Locate every uninfected red blood cell.
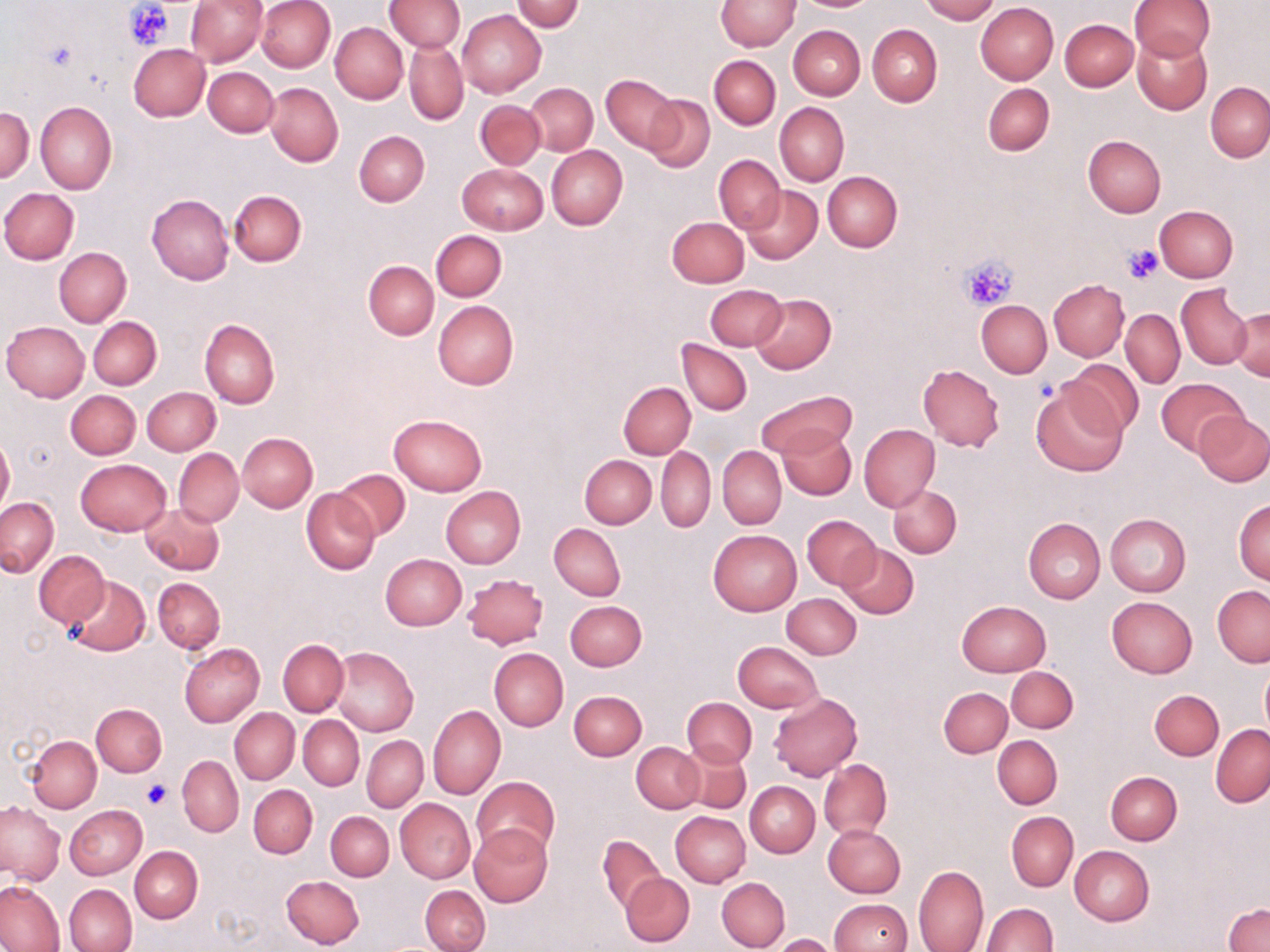
Approximate bounding boxes as (x1,y1)-(x2,y2) corner pairs in pixels.
Uninfected red blood cells: (185,0)-(266,66), (256,0)-(335,72), (920,0)-(998,23), (1130,0)-(1215,62), (384,1)-(464,53), (512,1)-(584,32), (715,1)-(799,50), (976,3)-(1059,84), (458,9)-(546,97), (1060,18)-(1138,91), (330,22)-(408,103), (789,25)-(865,99), (867,25)-(942,106), (1133,35)-(1213,115), (405,39)-(468,126), (128,44)-(210,121), (709,55)-(779,129), (204,67)-(278,137), (601,75)-(680,153), (982,82)-(1055,156), (1205,82)-(1270,162), (265,83)-(343,167), (526,83)-(597,155), (643,94)-(714,172), (475,100)-(545,169), (35,101)-(115,194), (775,102)-(849,186), (0,106)-(32,184), (354,130)-(430,206), (1083,135)-(1166,216), (546,145)-(627,229), (714,155)-(785,233), (457,164)-(548,235), (822,171)-(902,252), (742,185)-(822,263), (0,188)-(78,264), (227,190)-(306,267), (146,194)-(234,284), (1154,205)-(1238,282), (666,216)-(749,286), (431,230)-(507,301), (53,247)-(131,328), (364,260)-(439,339), (1049,280)-(1128,360), (705,283)-(787,350), (1176,284)-(1252,369), (750,293)-(836,374), (976,299)-(1052,378), (433,301)-(519,390), (1230,306)-(1269,381), (1121,308)-(1185,388), (88,317)-(162,389), (199,319)-(279,408), (1,321)-(90,402), (677,339)-(752,416), (1063,359)-(1142,438), (916,365)-(1004,451), (1156,377)-(1247,456), (617,381)-(696,459), (1031,385)-(1125,476), (142,386)-(220,455), (756,389)-(855,460), (65,390)-(140,459), (68,391)-(147,529), (1195,410)-(1270,486), (389,413)-(488,496), (859,424)-(940,511), (779,427)-(855,500), (237,432)-(317,512), (0,435)-(14,516), (718,446)-(786,529), (656,447)-(715,533), (174,449)-(243,526), (580,454)-(656,529), (75,459)-(171,536), (333,468)-(410,540), (889,485)-(961,558), (440,487)-(524,568), (301,488)-(380,575), (1,498)-(58,576), (1233,499)-(1270,585), (140,502)-(224,575), (1105,514)-(1190,596), (802,515)-(880,589), (1023,518)-(1105,603), (549,524)-(626,601), (708,529)-(802,617), (838,546)-(918,618), (35,550)-(109,627), (380,554)-(466,630), (463,572)-(549,649), (63,574)-(150,656), (153,577)-(225,653), (1212,585)-(1270,668), (782,593)-(862,659), (1106,596)-(1197,679), (565,600)-(647,671), (957,600)-(1050,675), (278,640)-(348,716), (733,641)-(823,714), (179,643)-(265,727), (330,647)-(419,737), (488,648)-(568,731), (1260,662)-(1270,736), (1006,666)-(1078,733), (938,687)-(1012,757), (1149,689)-(1224,760), (568,690)-(646,760), (769,692)-(862,782), (682,697)-(756,768), (91,703)-(167,776), (428,704)-(505,800), (230,707)-(299,784), (299,715)-(364,789), (1211,724)-(1270,807), (26,735)-(101,811), (992,735)-(1061,808), (362,736)-(428,812), (632,742)-(703,813), (678,743)-(751,814), (177,756)-(243,836), (819,758)-(892,841), (1105,771)-(1182,845), (472,776)-(558,858), (745,781)-(820,857), (249,785)-(317,857), (395,799)-(475,884), (0,802)-(64,885), (65,805)-(147,879), (326,812)-(393,880), (671,812)-(750,887), (1006,812)-(1078,890), (822,823)-(905,898), (469,824)-(553,908), (598,835)-(667,915), (129,846)-(202,923), (1070,846)-(1154,925), (914,865)-(988,952), (621,873)-(694,947), (280,874)-(365,949), (716,877)-(790,952), (0,881)-(64,951), (64,884)-(136,951), (420,885)-(490,952), (829,898)-(911,951), (981,902)-(1056,951), (1224,903)-(1270,951), (771,934)-(836,952).

Platelet locations: (126,1)-(172,49), (45,41)-(75,73), (1122,245)-(1164,283), (959,254)-(1018,311), (143,781)-(171,809). Slide-level diagnosis: no evidence of blood parasites. May-Grünwald-Giemsa-stained preparation. Image is 1270×952 pixels. Single field of view. Optical microscopy. 1000x magnification. Thin blood smear.